Assess this cell for malaria.
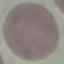

Uninfected.

preparation: thin blood smear
stain: Giemsa
capture: smartphone through the microscope eyepiece
image_type: cell patch, automatically extracted from a larger field of view and resized to 64 × 64 pixels